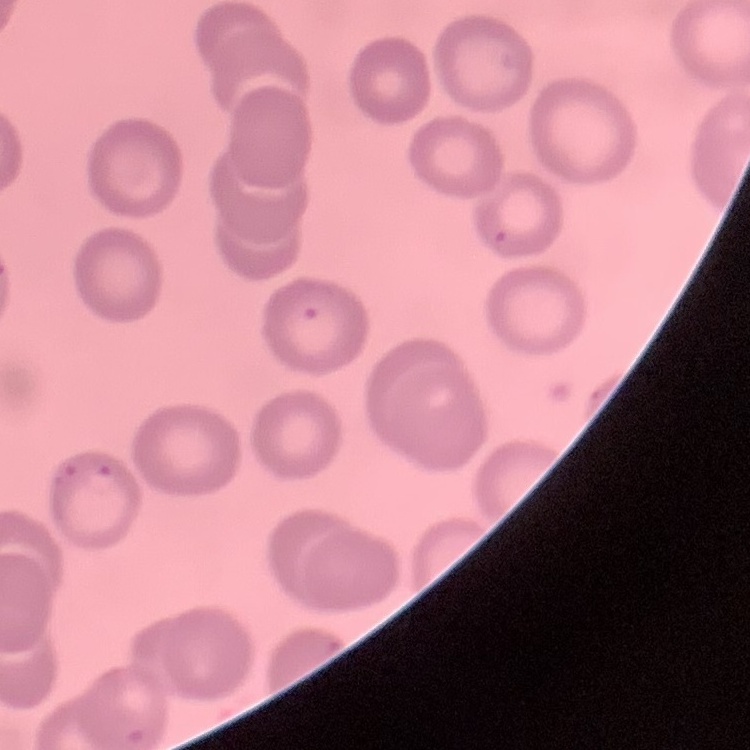

erythrocyte_morphology: no rouleaux formation
image_type: square crop of a larger photomicrograph
stain: Field's or Giemsa
preparation: thin blood film